Identify the preparation type.
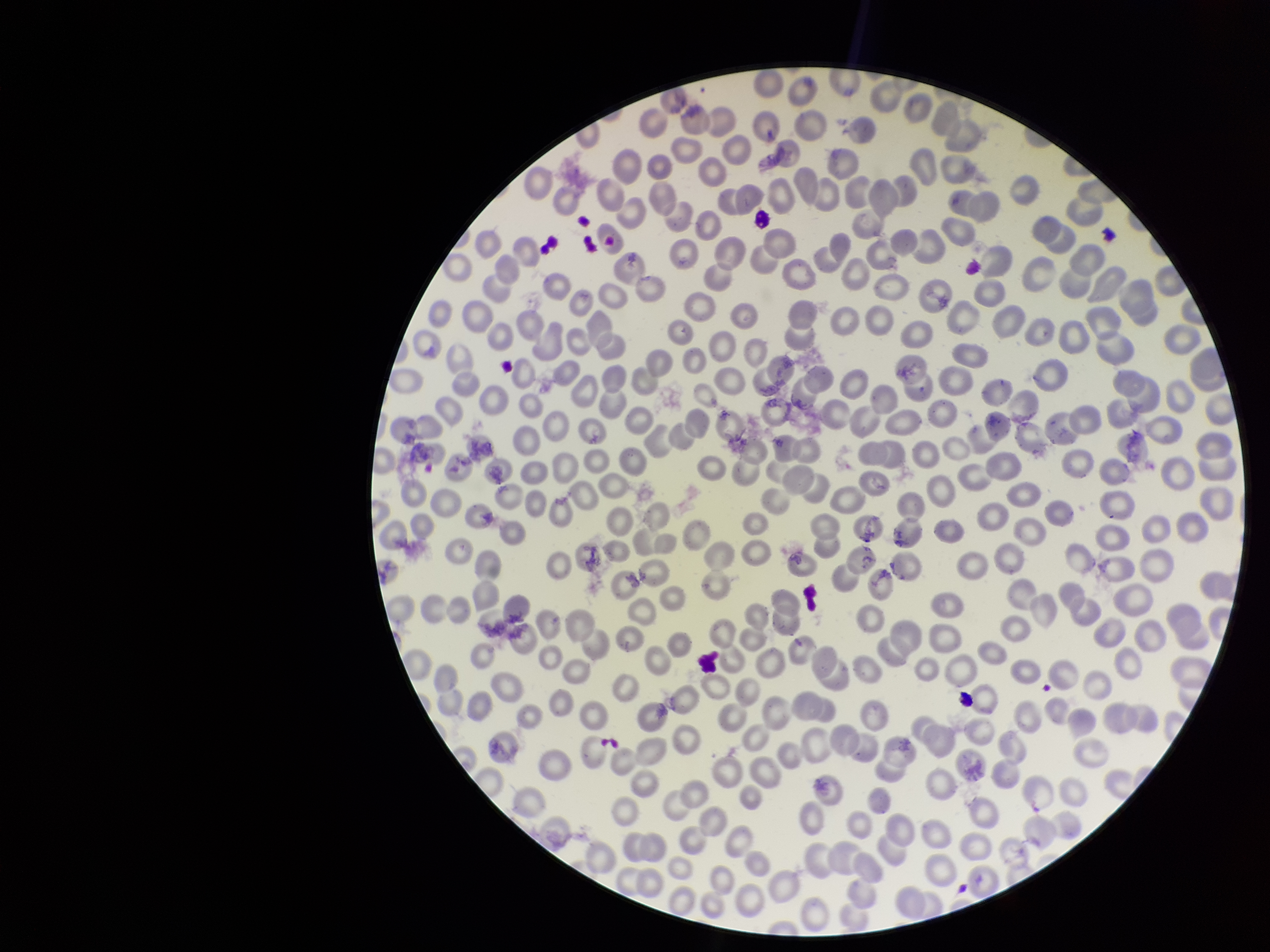

It is a thin blood smear.

Smartphone photograph taken through the eyepiece of a microscope. Giemsa stain. One field from this slide. Image is 1270×952 pixels. Patient malaria status: negative. Parasitized red blood cell count: 0. Red blood cell count: 291. Parasitized red blood cells: none detected.